Comment on the morphology of the erythrocytes.
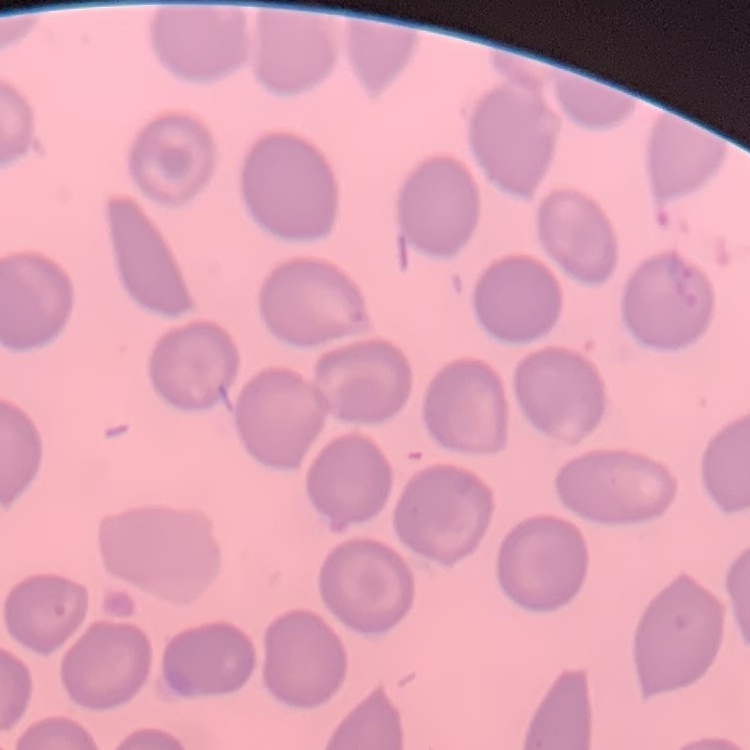
They show no rouleaux formation.

Summary:
  - Image type: one tile cut from a larger photomicrograph
  - Preparation: thin blood smear
  - Stain: Field's or Giemsa